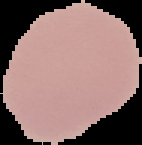
Summary:
  - Image type: segmented cell region with the area outside set to black
  - Image size: 142×145 pixels
  - Result: negative for Plasmodium parasites
  - Preparation: thin blood smear